State the preparation type.
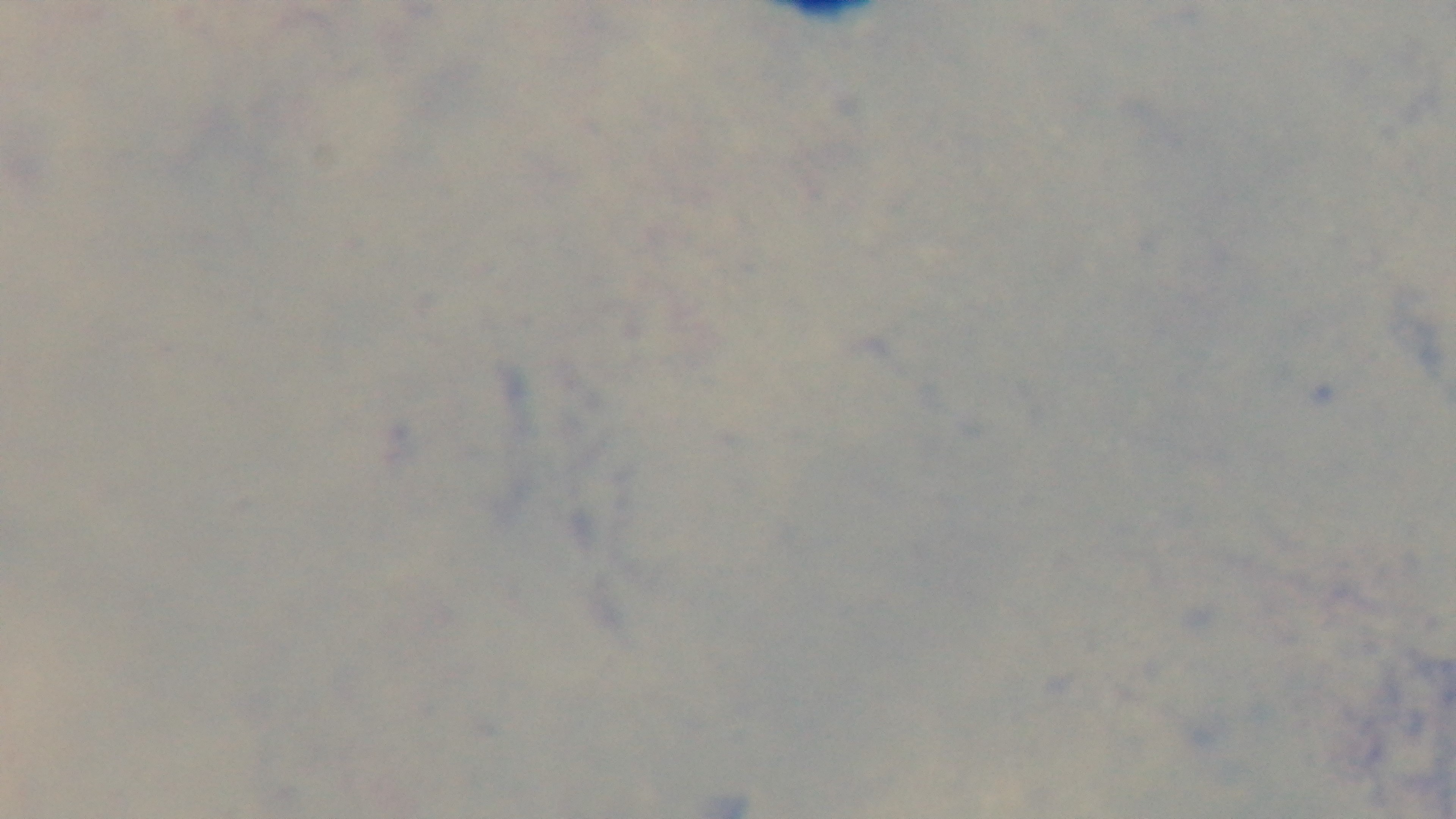
Thick.

Oil-immersion objective, 100x. Mounted 4K digital camera. Giemsa stain. Malaria status: uninfected. Photomicrograph. One field from the slide.